Evaluate for malaria.
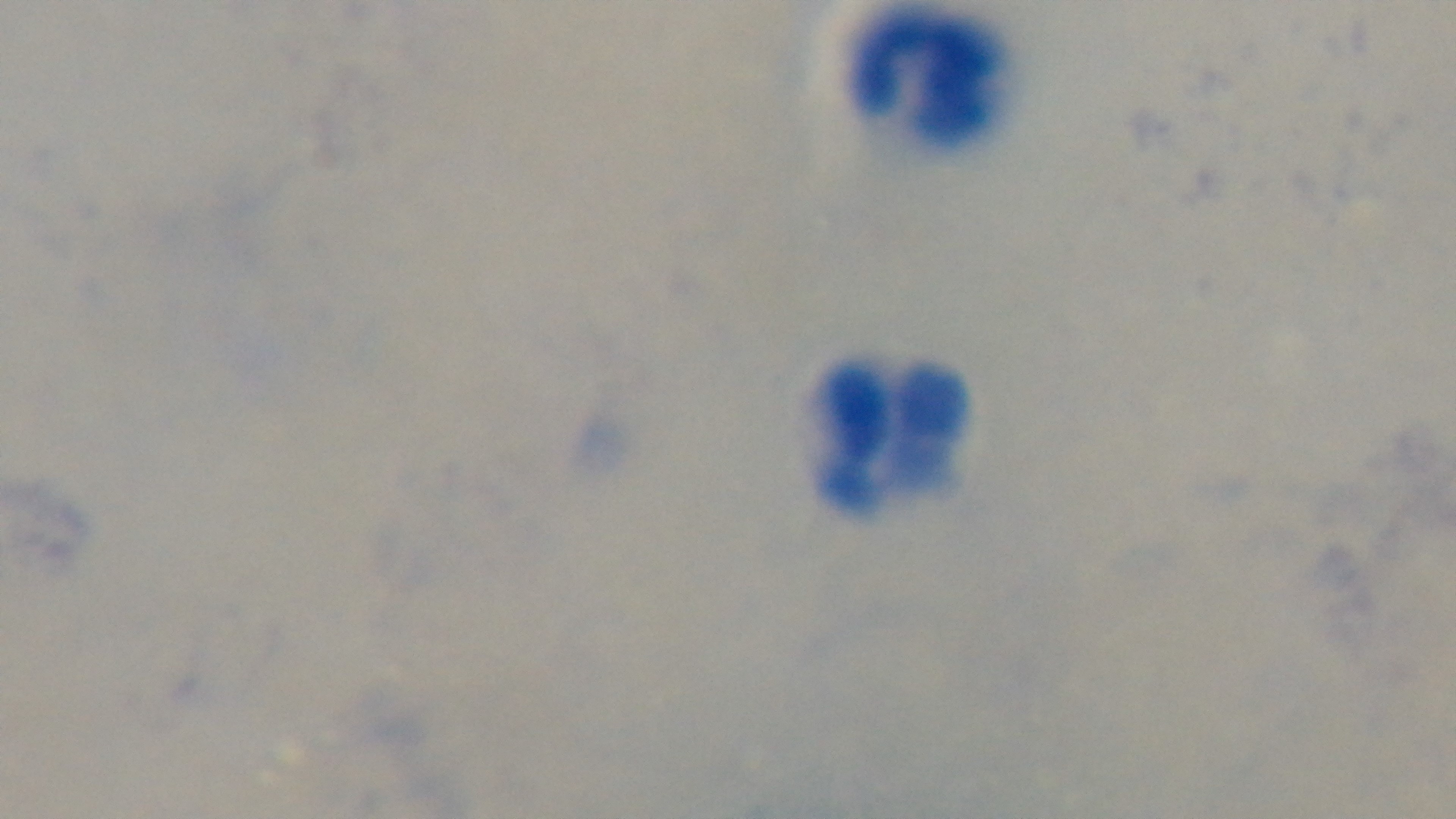
Uninfected.

Photomicrograph. Mounted 4K digital camera. Preparation: thick smear. One field from the slide. Oil-immersion objective, 100x. Giemsa stain.